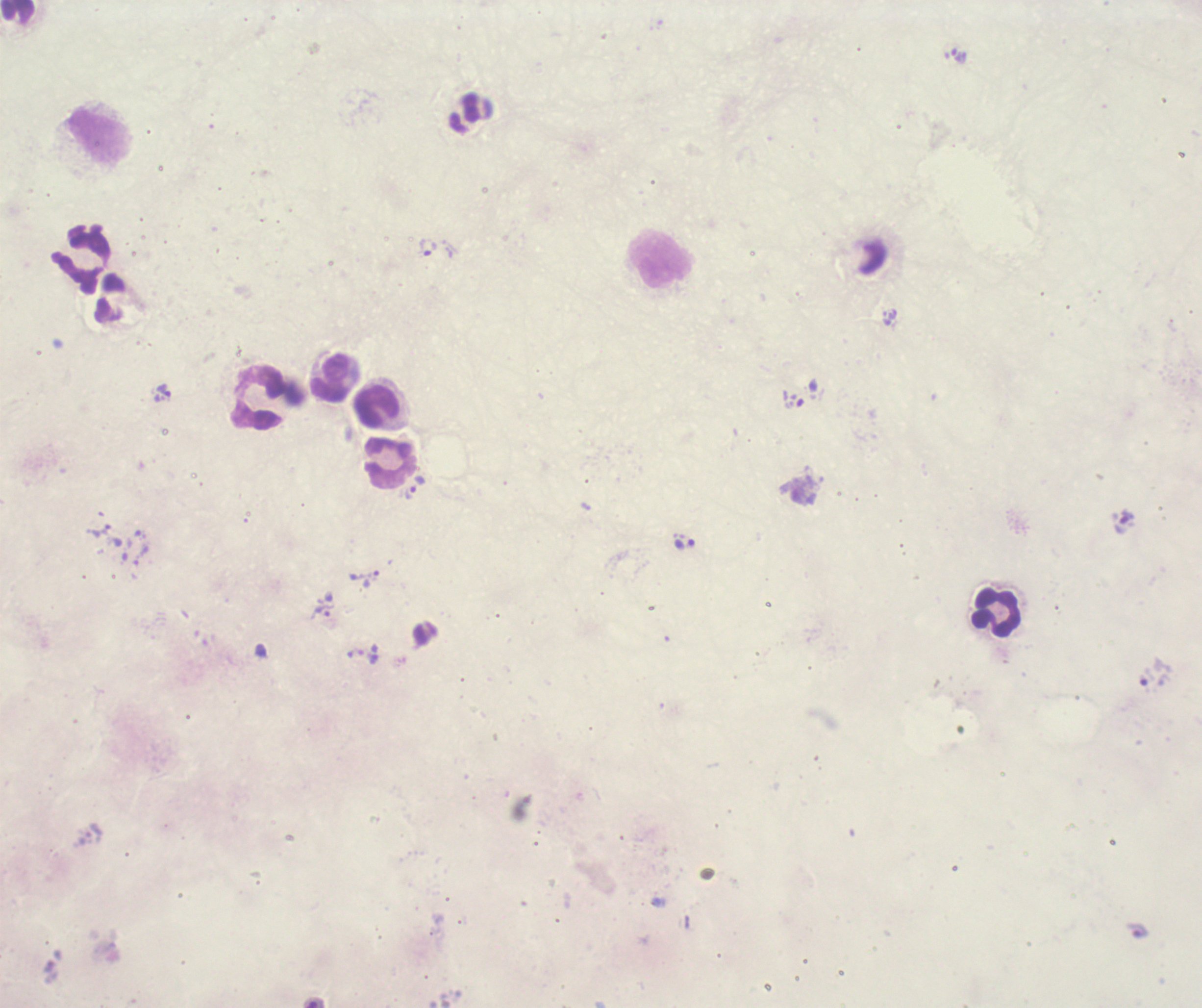

coordinate format = approximate centers as [x, y] in pixels
trophozoite locations = [959, 56], [428, 248], [164, 391], [685, 543], [324, 611], [1147, 679]
leukocyte locations = [18, 12], [101, 137], [82, 257], [660, 258], [330, 378], [258, 399], [377, 407], [390, 463], [996, 613]
coloration quality = bad
image size = 1202×1008 pixels
field of view = one from this slide
preparation = thick smear of blood
stain = Romanowsky
context = previously used in a real diagnosis
background quality = poor
magnification = 100x
result = Plasmodium parasites identified